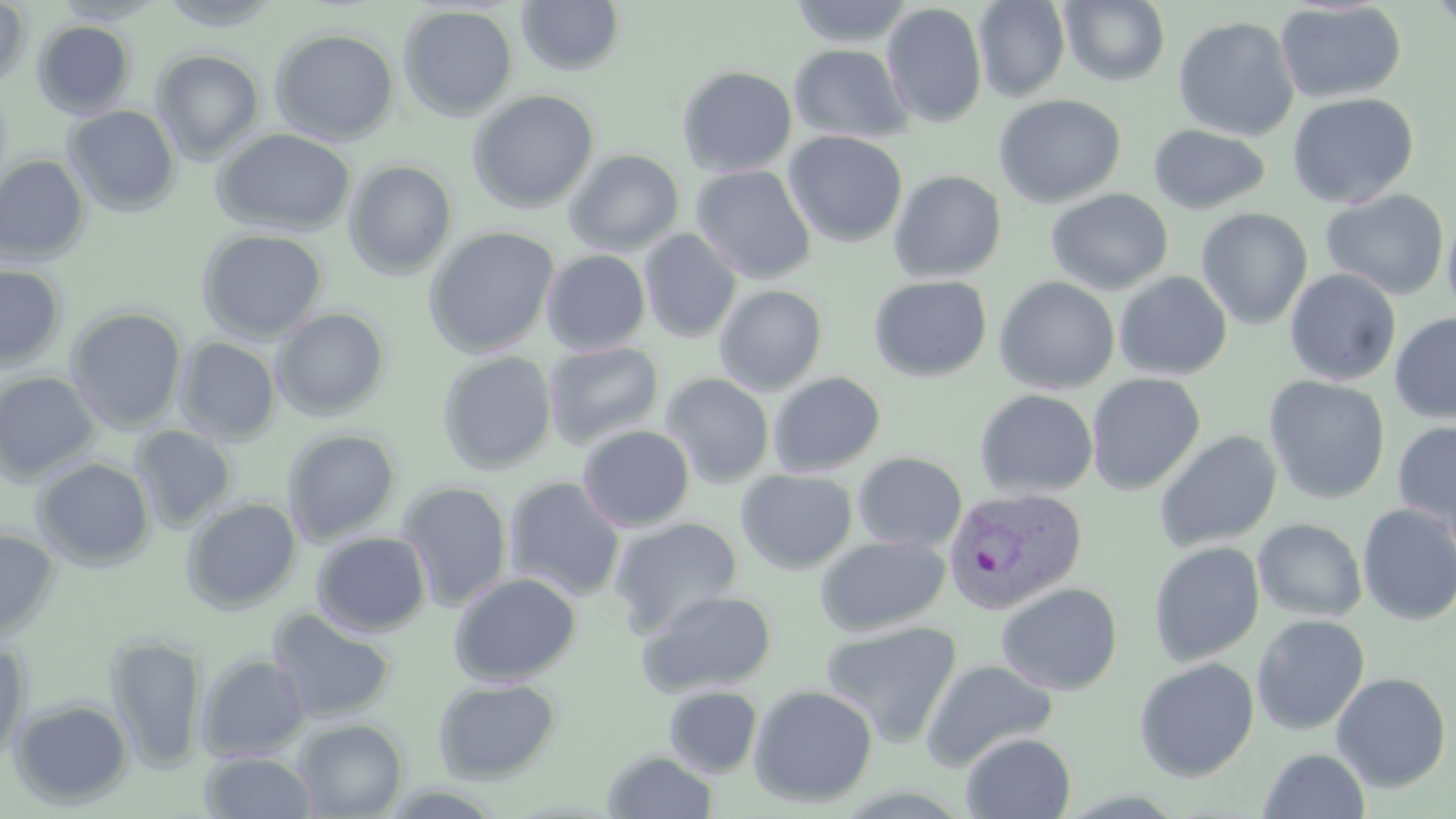
Approximate bounding boxes as [x1, y1, x2, y2] in pixels. Plasmodium vivax-infected red blood cell locations: [942, 486, 1088, 615]. Uninfected red blood cell locations: [0, 0, 31, 89], [155, 0, 284, 31], [788, 0, 915, 47], [973, 0, 1070, 102], [1059, 0, 1171, 86], [1427, 0, 1456, 38], [516, 1, 625, 77], [1274, 1, 1407, 104], [881, 2, 987, 129], [398, 4, 518, 121], [1173, 16, 1300, 141], [32, 20, 135, 119], [270, 27, 400, 145], [788, 43, 913, 144], [151, 49, 265, 164], [677, 65, 798, 177], [466, 90, 600, 213], [1287, 92, 1419, 208], [993, 94, 1125, 208], [64, 105, 180, 216], [1148, 124, 1271, 215], [212, 128, 356, 236], [783, 131, 907, 248], [565, 149, 685, 256], [0, 154, 91, 265], [343, 160, 458, 280], [690, 164, 815, 284], [889, 170, 1007, 283], [1045, 188, 1173, 295], [1322, 189, 1449, 300], [1195, 208, 1313, 330], [1442, 210, 1456, 321], [423, 226, 560, 358], [196, 229, 328, 342], [639, 229, 742, 343], [541, 249, 651, 355], [0, 264, 66, 369], [1284, 269, 1401, 386], [1113, 271, 1232, 381], [868, 275, 992, 382], [994, 276, 1120, 394], [714, 285, 827, 395], [66, 306, 188, 433], [271, 307, 391, 420], [1389, 313, 1456, 424], [175, 337, 282, 445], [543, 341, 665, 449], [437, 351, 557, 475], [0, 371, 102, 485], [768, 371, 885, 476], [659, 373, 774, 488], [1085, 373, 1205, 495], [1265, 376, 1390, 504], [974, 388, 1099, 499], [1392, 421, 1456, 541], [130, 425, 236, 533], [577, 425, 695, 532], [282, 428, 401, 545], [1154, 430, 1282, 552], [852, 452, 968, 553], [32, 458, 155, 571], [736, 469, 858, 574], [503, 477, 626, 601], [395, 481, 513, 611], [182, 497, 302, 613], [1357, 503, 1456, 626], [608, 517, 743, 638], [1253, 518, 1367, 622], [0, 528, 60, 640], [311, 531, 432, 636], [815, 535, 951, 637], [1148, 541, 1266, 667], [449, 572, 581, 686], [996, 582, 1123, 695], [635, 587, 777, 697], [266, 607, 396, 724], [1250, 614, 1370, 735], [821, 620, 962, 747], [104, 633, 208, 771], [0, 641, 30, 765], [197, 653, 311, 761], [1133, 657, 1260, 782], [921, 658, 1058, 770], [1331, 672, 1452, 793], [432, 676, 561, 783], [748, 684, 878, 808], [663, 685, 763, 778], [8, 698, 134, 809], [293, 718, 407, 818], [961, 731, 1077, 818], [1258, 748, 1370, 818], [199, 750, 318, 818], [603, 750, 718, 818]. Slide-level diagnosis: Plasmodium vivax. Captured at 1000x magnification. May-Grünwald-Giemsa stain. Single field of view. Image is 1456×819 pixels. Light microscopy. Thin blood film.